Classify this cell by malaria status.
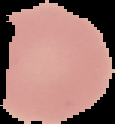
Uninfected.

image size = 115×124 pixels
preparation = thin blood smear
image type = cell region segmented out of the field of view; surrounding area masked to black